Identify the parasite.
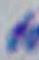
This is Toxoplasma gondii.

Captured at 1000x magnification. Micrograph.